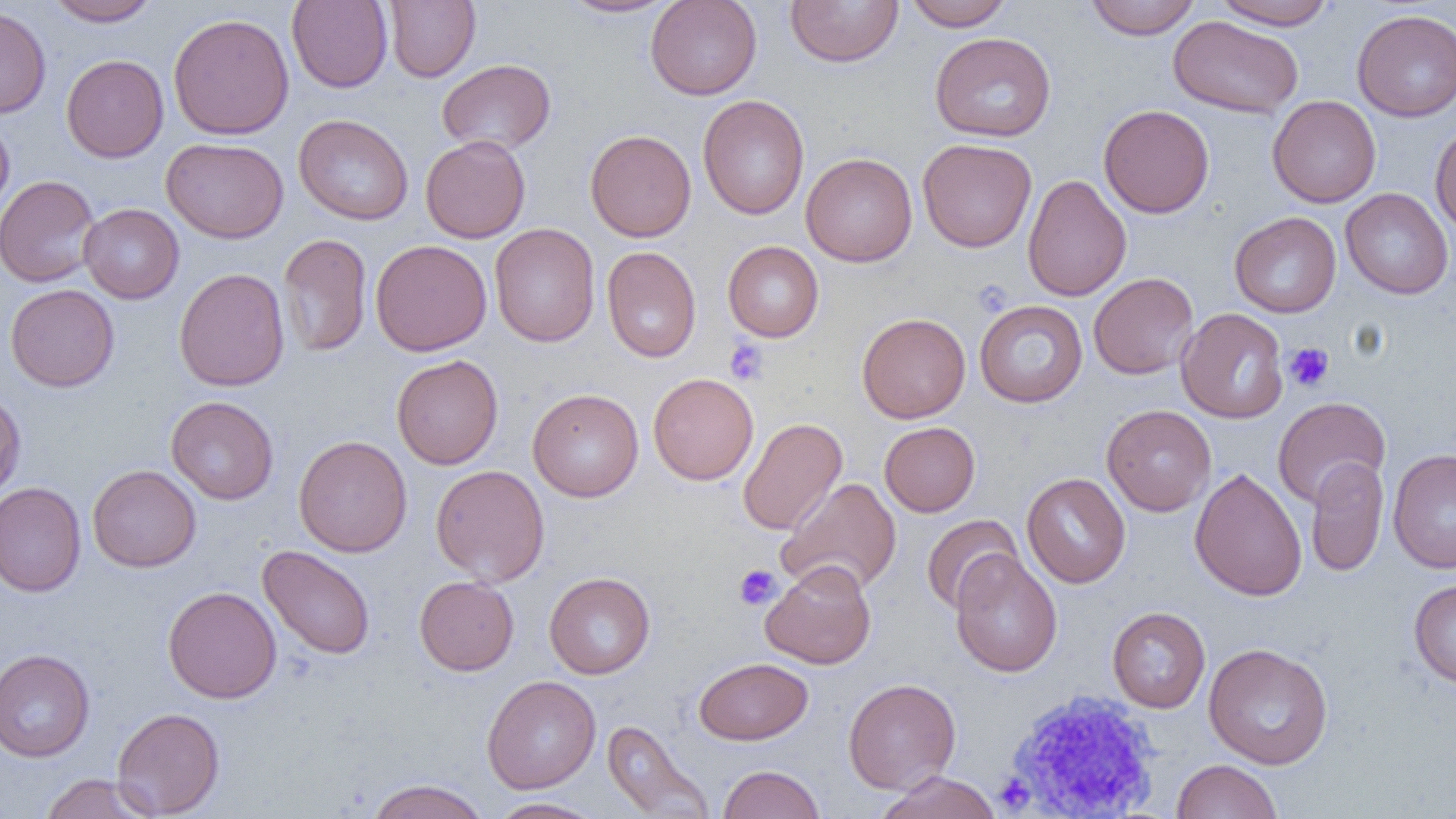 Approximate bounding boxes as (x1,y1)-(x2,y2) corner pairs in pixels. Uninfected red blood cell locations: (46,0)-(160,26), (287,0)-(393,92), (384,0)-(480,82), (558,0)-(682,18), (645,0)-(762,100), (904,0)-(1014,31), (1085,0)-(1201,40), (1212,0)-(1337,30), (784,1)-(904,67), (0,5)-(51,118), (1352,9)-(1456,121), (168,13)-(295,140), (1168,16)-(1303,119), (929,32)-(1056,142), (61,54)-(168,162), (436,59)-(556,155), (697,95)-(810,220), (1267,95)-(1381,208), (1098,104)-(1214,218), (0,114)-(15,220), (293,114)-(414,225), (1430,122)-(1456,236), (585,129)-(696,242), (420,135)-(530,243), (161,137)-(288,243), (917,138)-(1037,252), (800,152)-(917,267), (1022,174)-(1132,302), (0,175)-(101,288), (1340,188)-(1454,299), (79,203)-(184,304), (1229,212)-(1341,318), (489,223)-(600,347), (277,233)-(372,357), (370,240)-(492,356), (722,241)-(824,342), (602,246)-(701,363), (173,268)-(290,391), (1088,272)-(1199,379), (5,284)-(119,392), (974,300)-(1088,407), (1175,308)-(1289,423), (857,312)-(971,423), (391,354)-(504,470), (648,372)-(759,485), (527,388)-(644,502), (0,391)-(26,500), (165,396)-(279,505), (1272,396)-(1391,507), (1102,404)-(1216,516), (737,417)-(848,535), (879,422)-(980,516), (294,435)-(412,558), (1388,447)-(1456,573), (1305,458)-(1389,577), (87,464)-(202,572), (431,464)-(549,586), (1189,467)-(1307,601), (1021,472)-(1131,588), (778,477)-(902,596), (0,481)-(86,597), (921,515)-(1022,614), (258,545)-(375,659), (950,548)-(1063,678), (760,560)-(876,669), (543,571)-(655,679), (414,575)-(519,675), (1408,579)-(1456,688), (163,586)-(281,704), (1107,607)-(1211,712), (1203,643)-(1333,769), (0,648)-(95,762), (694,657)-(813,745), (482,675)-(601,793), (843,678)-(961,794), (112,707)-(225,817), (601,719)-(713,819), (1171,759)-(1282,818), (717,764)-(825,819), (875,771)-(1001,819), (39,773)-(160,819), (364,779)-(491,819), (487,797)-(605,819). White blood cell locations: (1002,690)-(1164,817). Platelet locations: (971,279)-(1013,318), (724,339)-(769,386), (1284,342)-(1335,392), (734,564)-(782,610), (995,773)-(1035,812). Slide-level diagnosis: negative for blood parasites. Thin blood smear. Captured at 1000x magnification. Image is 1456×819 pixels. Light microscopy. Single field of view.